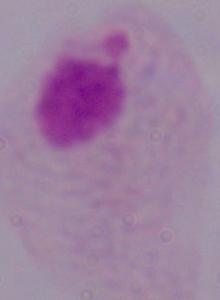 Captured at 1000x magnification. A trichomonad is shown. Photomicrograph.